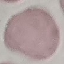

result: no malaria parasites detected
capture: smartphone camera at the microscope eyepiece
image_type: cell patch, automatically extracted from a larger field of view and resized to 64 × 64 pixels
preparation: thin smear
stain: Giemsa